Locate every uninfected red blood cell.
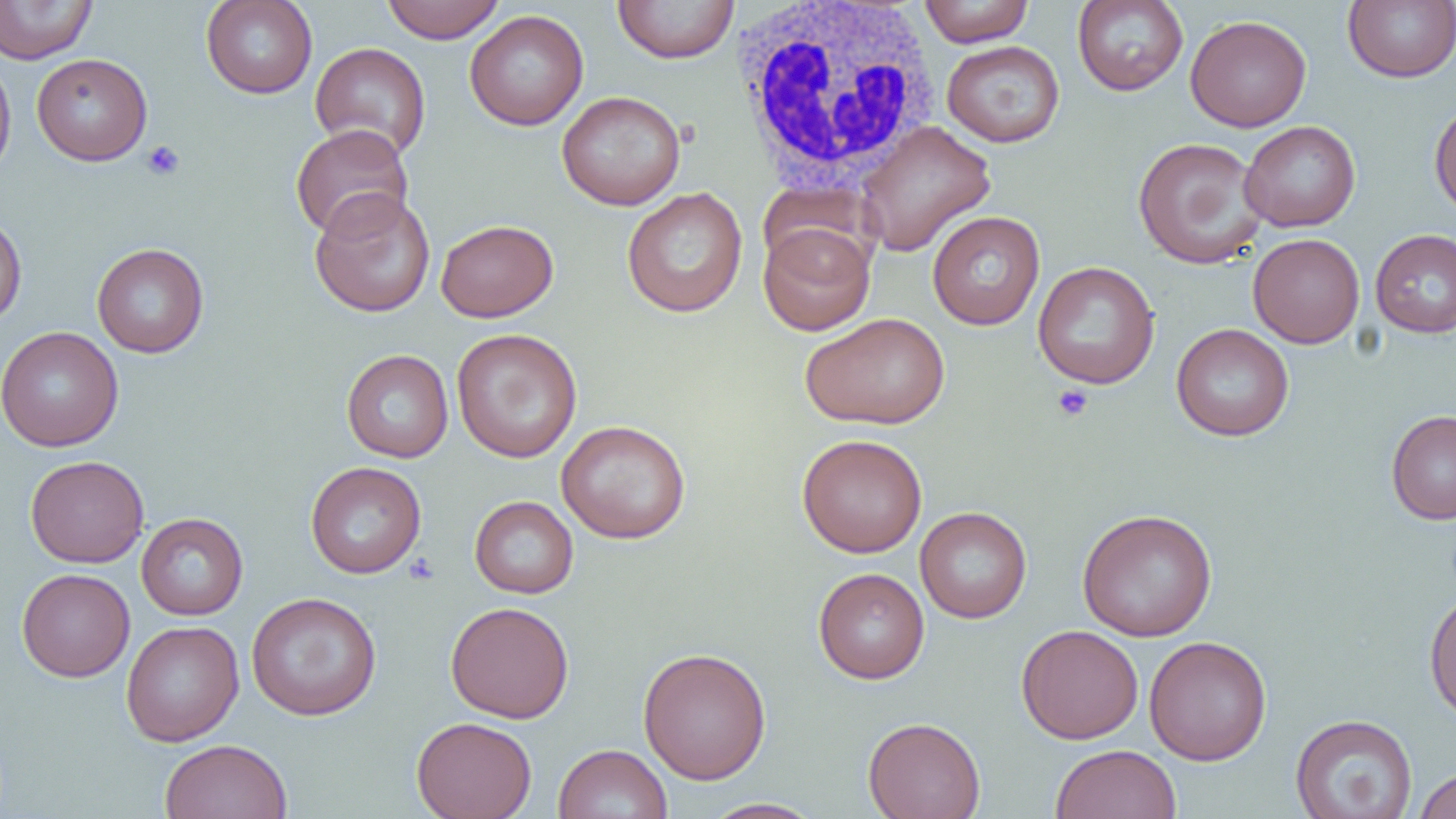
Approximate bounding boxes as named x1/y1/x2/y2 corners in pixels.
Uninfected red blood cells: (x1=201, y1=0, x2=318, y2=99), (x1=380, y1=0, x2=507, y2=43), (x1=612, y1=0, x2=740, y2=64), (x1=918, y1=0, x2=1034, y2=46), (x1=1072, y1=0, x2=1189, y2=96), (x1=1343, y1=0, x2=1456, y2=83), (x1=0, y1=1, x2=97, y2=64), (x1=464, y1=9, x2=589, y2=131), (x1=1185, y1=14, x2=1312, y2=132), (x1=941, y1=40, x2=1065, y2=147), (x1=309, y1=42, x2=432, y2=161), (x1=31, y1=53, x2=153, y2=166), (x1=0, y1=54, x2=17, y2=183), (x1=556, y1=90, x2=686, y2=211), (x1=1429, y1=98, x2=1456, y2=220), (x1=855, y1=120, x2=996, y2=257), (x1=1239, y1=120, x2=1361, y2=232), (x1=289, y1=124, x2=414, y2=240), (x1=1132, y1=136, x2=1268, y2=269), (x1=309, y1=187, x2=436, y2=318), (x1=621, y1=187, x2=748, y2=318), (x1=927, y1=211, x2=1045, y2=330), (x1=0, y1=212, x2=27, y2=328), (x1=435, y1=218, x2=559, y2=322), (x1=758, y1=221, x2=876, y2=335), (x1=1370, y1=228, x2=1456, y2=338), (x1=1248, y1=232, x2=1365, y2=349), (x1=91, y1=243, x2=209, y2=358), (x1=1033, y1=261, x2=1160, y2=389), (x1=800, y1=311, x2=950, y2=430), (x1=1171, y1=323, x2=1294, y2=442), (x1=0, y1=326, x2=124, y2=451), (x1=451, y1=328, x2=583, y2=463), (x1=341, y1=349, x2=454, y2=463), (x1=1386, y1=409, x2=1456, y2=524), (x1=556, y1=418, x2=691, y2=544), (x1=796, y1=433, x2=928, y2=558), (x1=25, y1=455, x2=149, y2=568), (x1=305, y1=461, x2=426, y2=578), (x1=469, y1=495, x2=579, y2=598), (x1=915, y1=506, x2=1032, y2=623), (x1=1077, y1=508, x2=1218, y2=641), (x1=136, y1=513, x2=248, y2=620), (x1=813, y1=567, x2=929, y2=684), (x1=17, y1=568, x2=135, y2=682), (x1=1424, y1=590, x2=1456, y2=722), (x1=246, y1=592, x2=382, y2=720), (x1=445, y1=601, x2=574, y2=723), (x1=121, y1=621, x2=244, y2=746), (x1=1016, y1=624, x2=1144, y2=744), (x1=1144, y1=635, x2=1272, y2=765), (x1=638, y1=646, x2=772, y2=785), (x1=1290, y1=713, x2=1418, y2=819), (x1=411, y1=716, x2=537, y2=819), (x1=862, y1=716, x2=985, y2=819), (x1=159, y1=739, x2=292, y2=819), (x1=553, y1=743, x2=672, y2=819), (x1=1050, y1=744, x2=1182, y2=819), (x1=1412, y1=766, x2=1456, y2=819), (x1=701, y1=797, x2=825, y2=818).

Summary:
  - Platelet locations: (x1=141, y1=140, x2=185, y2=181), (x1=1051, y1=384, x2=1093, y2=422), (x1=404, y1=552, x2=439, y2=585)
  - White blood cell locations: (x1=728, y1=0, x2=943, y2=193)
  - Slide-level diagnosis: no evidence of blood parasites
  - Preparation: thin blood film
  - Magnification: 1000x
  - Image size: 1456×819 pixels
  - Modality: optical microscopy
  - Field of view: single